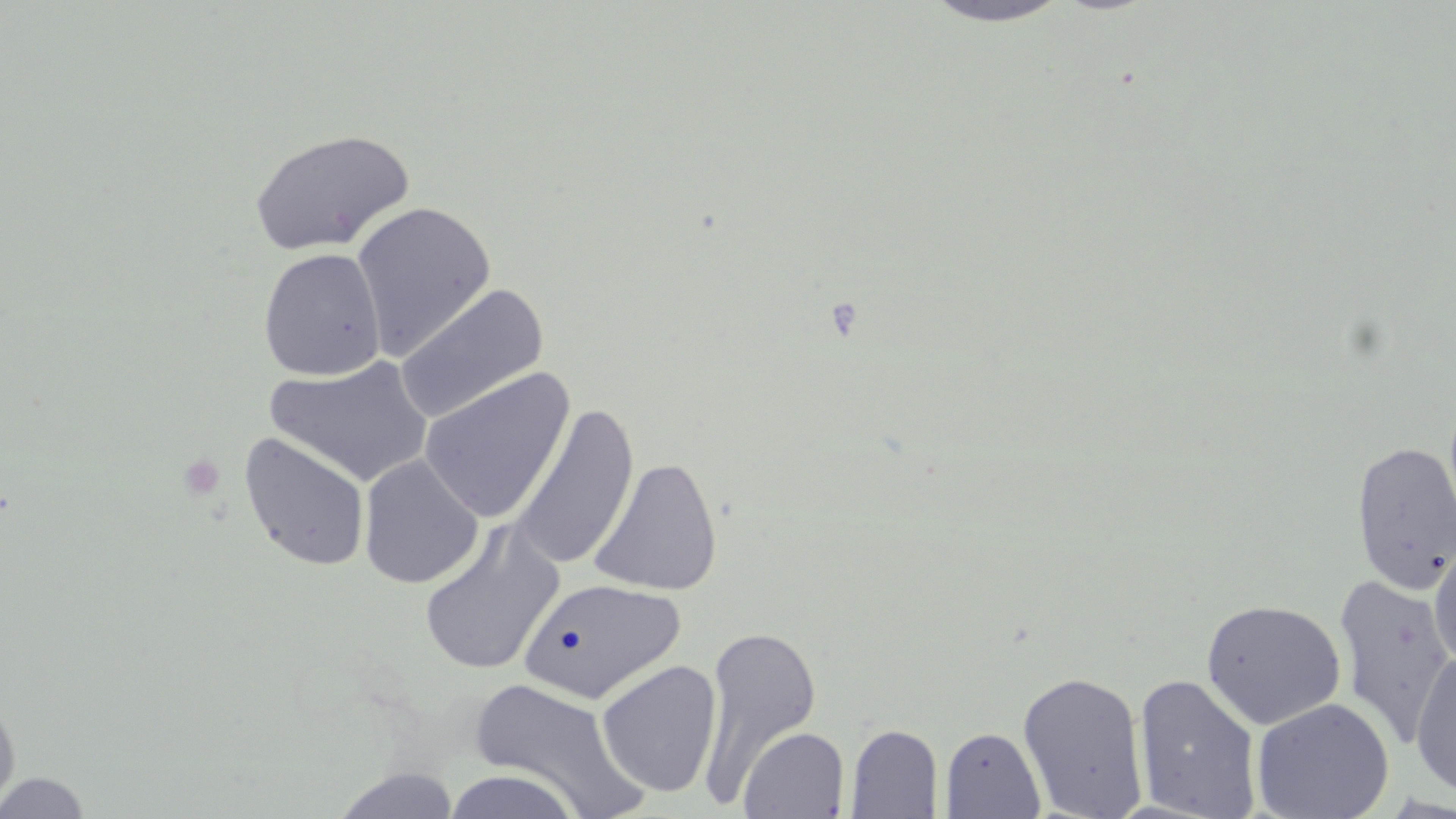

slide-level diagnosis = no evidence of blood parasites
field of view = single
preparation = thin blood film
platelet locations = approximate bounding boxes as (x1, y1, x2, y2) in pixels: (178, 453, 227, 501)
image size = 1456×819 pixels
stain = May-Grünwald-Giemsa
uninfected red blood cell locations = approximate bounding boxes as (x1, y1, x2, y2) in pixels: (920, 1, 1075, 28), (249, 128, 415, 256), (350, 200, 497, 359), (258, 248, 386, 381), (394, 284, 549, 424), (266, 356, 434, 488), (418, 367, 576, 524), (510, 403, 640, 571), (238, 432, 371, 572), (1351, 439, 1456, 594), (358, 455, 483, 589), (589, 457, 723, 596), (418, 521, 565, 676), (1428, 540, 1456, 671), (1333, 574, 1456, 745), (519, 579, 686, 703), (1200, 598, 1347, 731), (699, 624, 821, 800), (1411, 648, 1456, 797), (596, 660, 722, 797), (1017, 670, 1149, 818), (1133, 673, 1263, 818), (467, 676, 649, 818), (0, 691, 20, 816), (1252, 697, 1394, 819), (845, 724, 943, 818), (738, 726, 850, 818), (940, 726, 1045, 819), (332, 768, 460, 819), (442, 769, 584, 819), (0, 771, 93, 818)
modality = light microscopy
magnification = 1000x